Assess this cell for malaria.
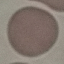
Uninfected.

Summary:
  - Preparation: thin blood film
  - Image type: automatically extracted cell patch, resized to 64 × 64 pixels
  - Stain: Giemsa
  - Capture: smartphone camera at the microscope eyepiece